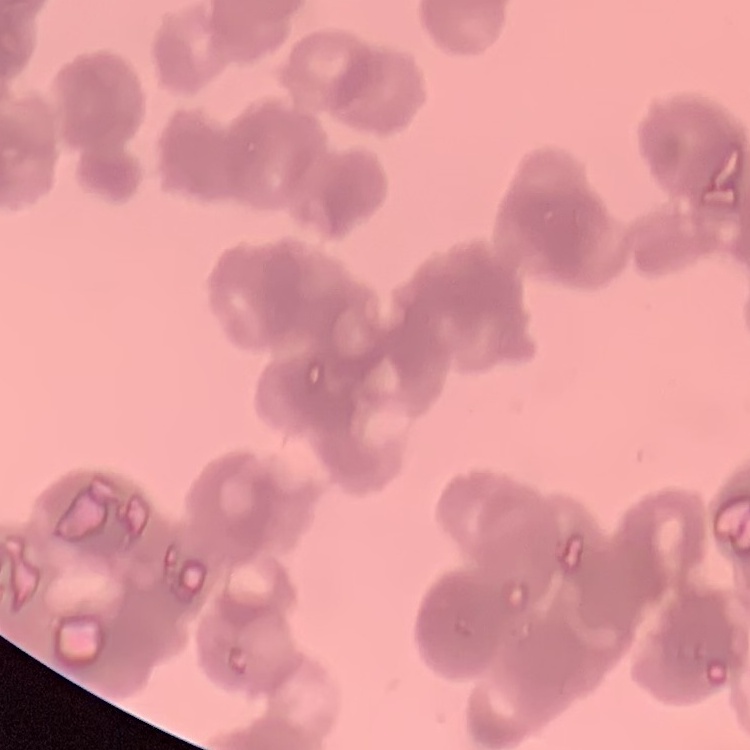
erythrocyte morphology = rouleaux formation
stain = Field's or Giemsa
preparation = thin blood smear
image type = one tile cut from a larger photomicrograph